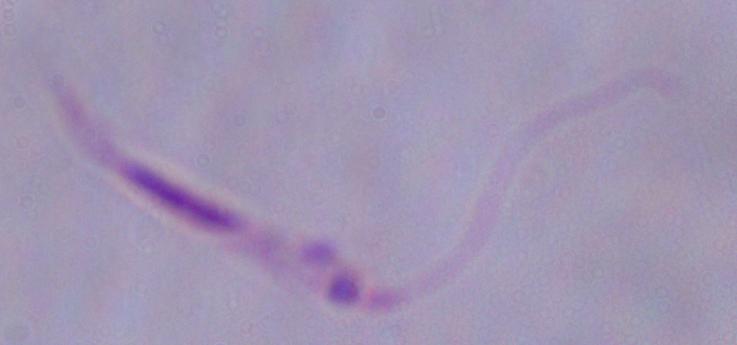
Summary:
  - Magnification: 1000x
  - Modality: micrograph
  - Identification: Leishmania